Identify the cell.
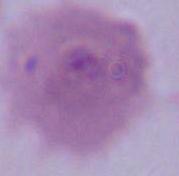

This is an erythrocyte.

Summary:
  - Modality: micrograph
  - Magnification: 1000x